Assess this cell for malaria.
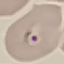
Parasitized.

Summary:
  - Stain: Giemsa
  - Image type: cell patch, automatically extracted from a larger field of view and resized to 64 × 64 pixels
  - Capture: smartphone through the microscope eyepiece
  - Preparation: thin blood smear